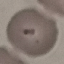

Malaria status: uninfected. Giemsa stain. Automatically extracted cell patch, resized to 64 × 64 pixels. Acquired by smartphone through the microscope eyepiece. Thin blood smear.